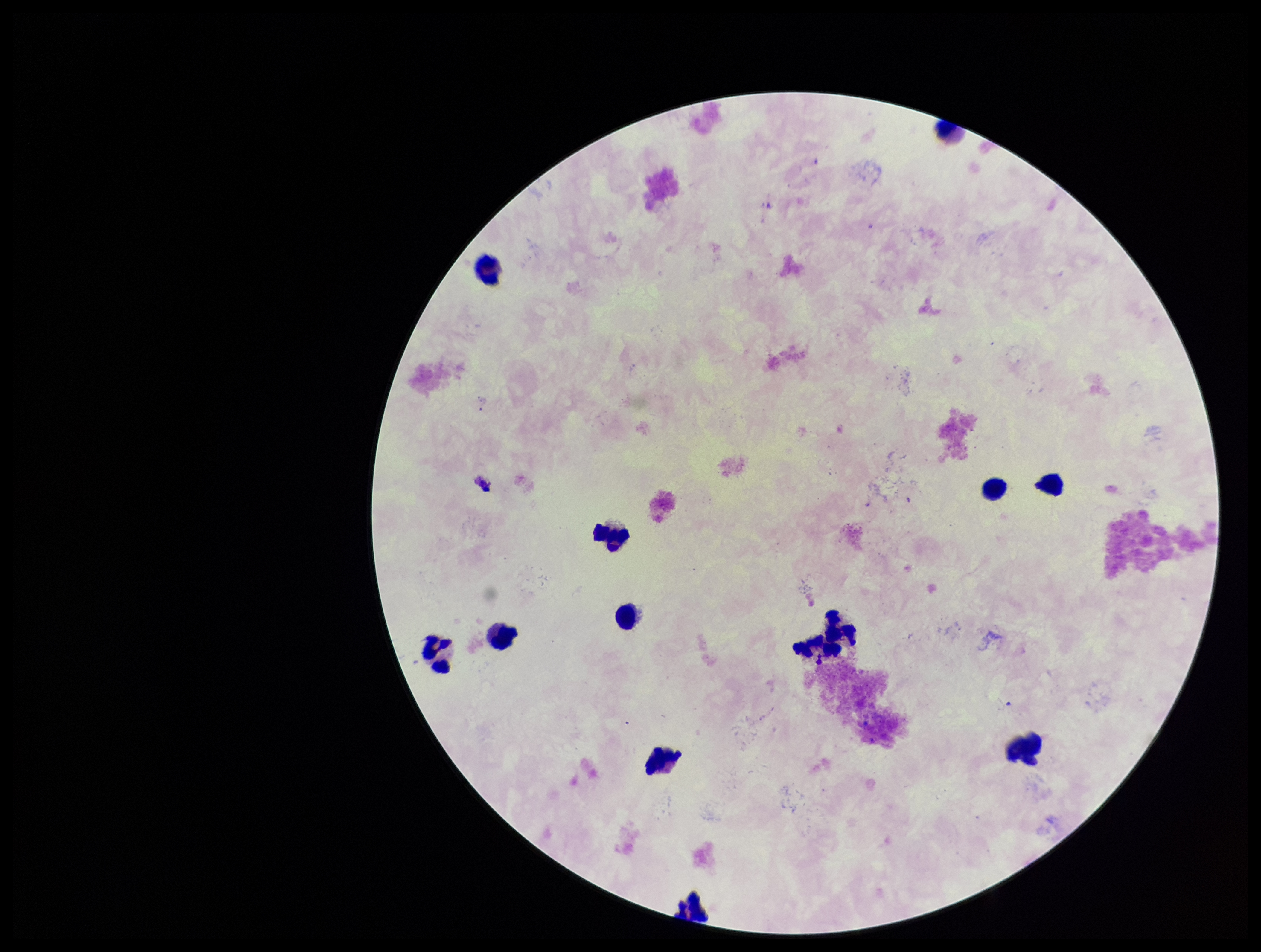 Single field of view. Giemsa stain. Plasmodium parasites: none detected. Patient malaria status: negative. Photographed through the microscope eyepiece with a smartphone camera. Image is 1261×952 pixels. Leukocyte count: 13. Parasite count: 0. Preparation: thick.